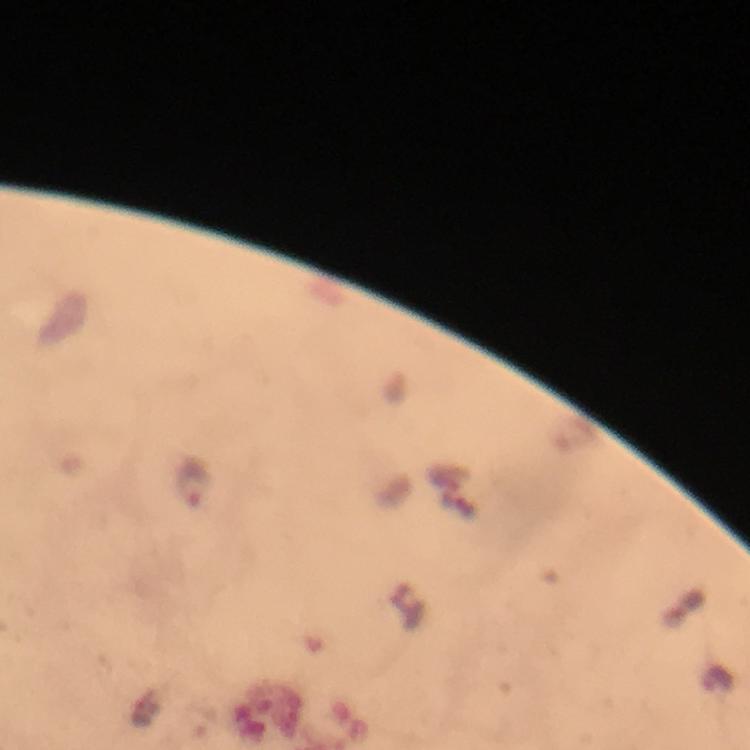
Approximate centers as {x, y} in pixels.
Summary:
  - Plasmodium parasite locations: {192, 483}
  - Image size: 750×750 pixels
  - Immersion oil: used
  - Context: from a diagnostic examination for malaria
  - Magnification: 100x
  - Preparation: thick blood film
  - Cropped from: a single field of view
  - Stain: Giemsa
  - Capture: smartphone photograph through a microscope